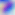

magnification = 400x
modality = photomicrograph
identification = Toxoplasma gondii